Comment on the morphology of the red blood cells.
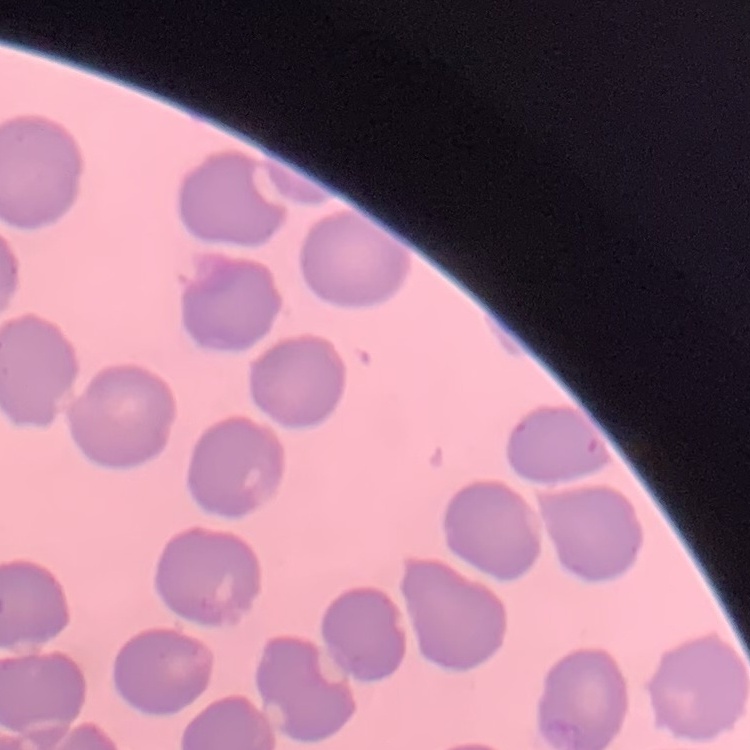
No rouleaux formation.

Summary:
  - Stain: Field's or Giemsa
  - Image type: one tile cut from a larger photomicrograph
  - Preparation: thin blood smear